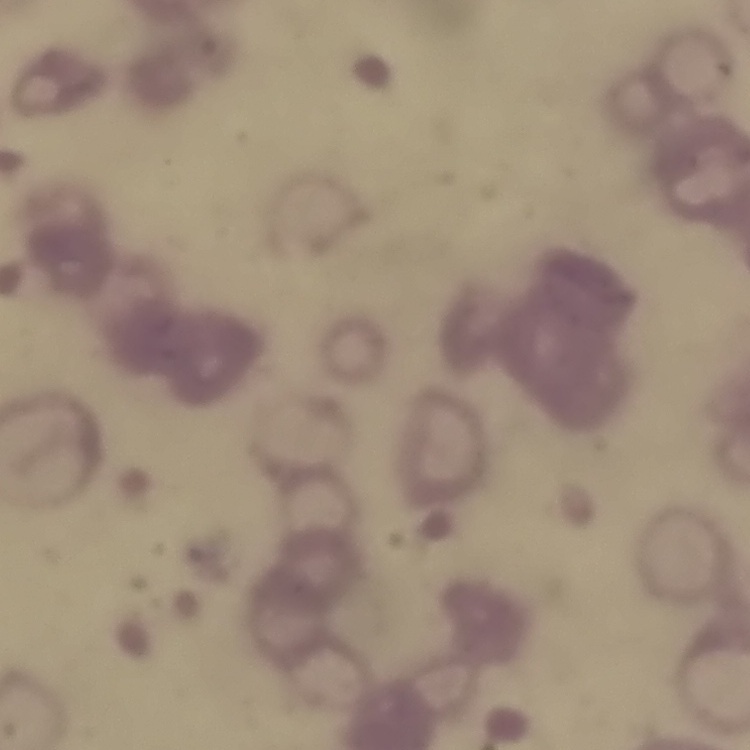
The red blood cells exhibit rouleaux formation. Square crop of a larger photomicrograph. Field's or Giemsa stain. Thin blood smear.